Locate and identify every blood parasite.
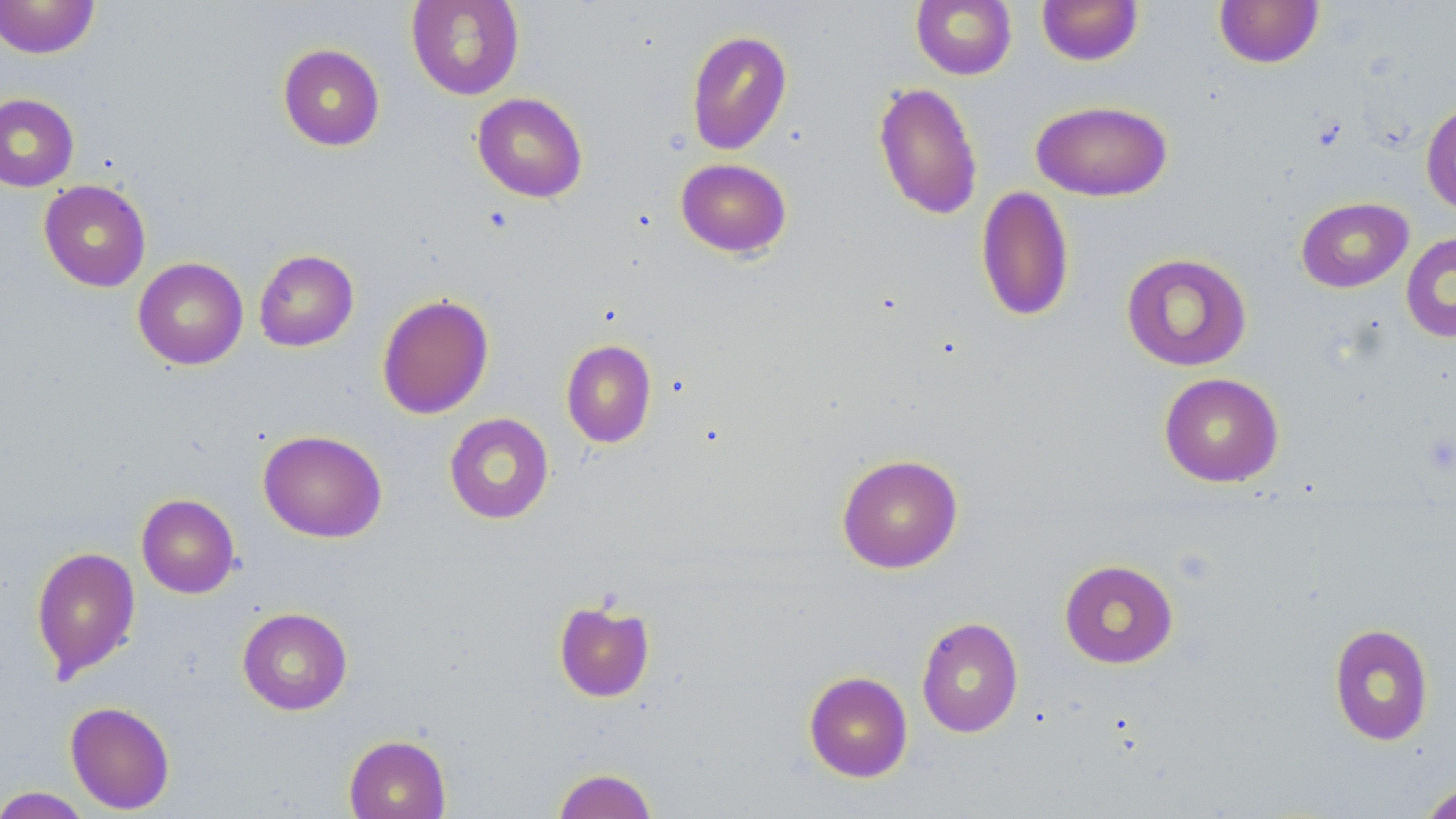

No blood parasites observed.

Approximate bounding boxes as named x1/y1/x2/y2 corners in pixels. Uninfected red blood cell locations: (x1=0, y1=0, x2=100, y2=59), (x1=406, y1=0, x2=525, y2=100), (x1=911, y1=0, x2=1017, y2=80), (x1=1036, y1=0, x2=1144, y2=66), (x1=1214, y1=0, x2=1324, y2=69), (x1=685, y1=29, x2=792, y2=156), (x1=277, y1=43, x2=385, y2=151), (x1=873, y1=82, x2=983, y2=220), (x1=0, y1=92, x2=79, y2=191), (x1=472, y1=92, x2=588, y2=203), (x1=1030, y1=99, x2=1174, y2=201), (x1=1420, y1=99, x2=1456, y2=216), (x1=676, y1=158, x2=792, y2=258), (x1=39, y1=179, x2=151, y2=292), (x1=975, y1=185, x2=1074, y2=323), (x1=1296, y1=197, x2=1414, y2=293), (x1=1401, y1=230, x2=1456, y2=343), (x1=254, y1=249, x2=359, y2=352), (x1=1121, y1=252, x2=1253, y2=371), (x1=133, y1=257, x2=248, y2=370), (x1=377, y1=293, x2=494, y2=420), (x1=561, y1=339, x2=657, y2=448), (x1=1159, y1=372, x2=1284, y2=487), (x1=443, y1=412, x2=554, y2=524), (x1=258, y1=430, x2=387, y2=543), (x1=836, y1=453, x2=963, y2=574), (x1=136, y1=493, x2=240, y2=598), (x1=30, y1=545, x2=141, y2=681), (x1=1059, y1=559, x2=1178, y2=669), (x1=553, y1=598, x2=656, y2=702), (x1=237, y1=607, x2=353, y2=715), (x1=916, y1=616, x2=1024, y2=737), (x1=1328, y1=623, x2=1434, y2=746), (x1=804, y1=671, x2=913, y2=782), (x1=65, y1=701, x2=175, y2=814), (x1=343, y1=734, x2=451, y2=819), (x1=551, y1=768, x2=657, y2=819), (x1=1418, y1=780, x2=1456, y2=819), (x1=0, y1=786, x2=93, y2=819). Slide-level diagnosis: negative for blood parasites. Image is 1456×819 pixels. Optical microscopy. Thin blood smear. Single field of view. 1000x magnification. May-Grünwald-Giemsa stain.